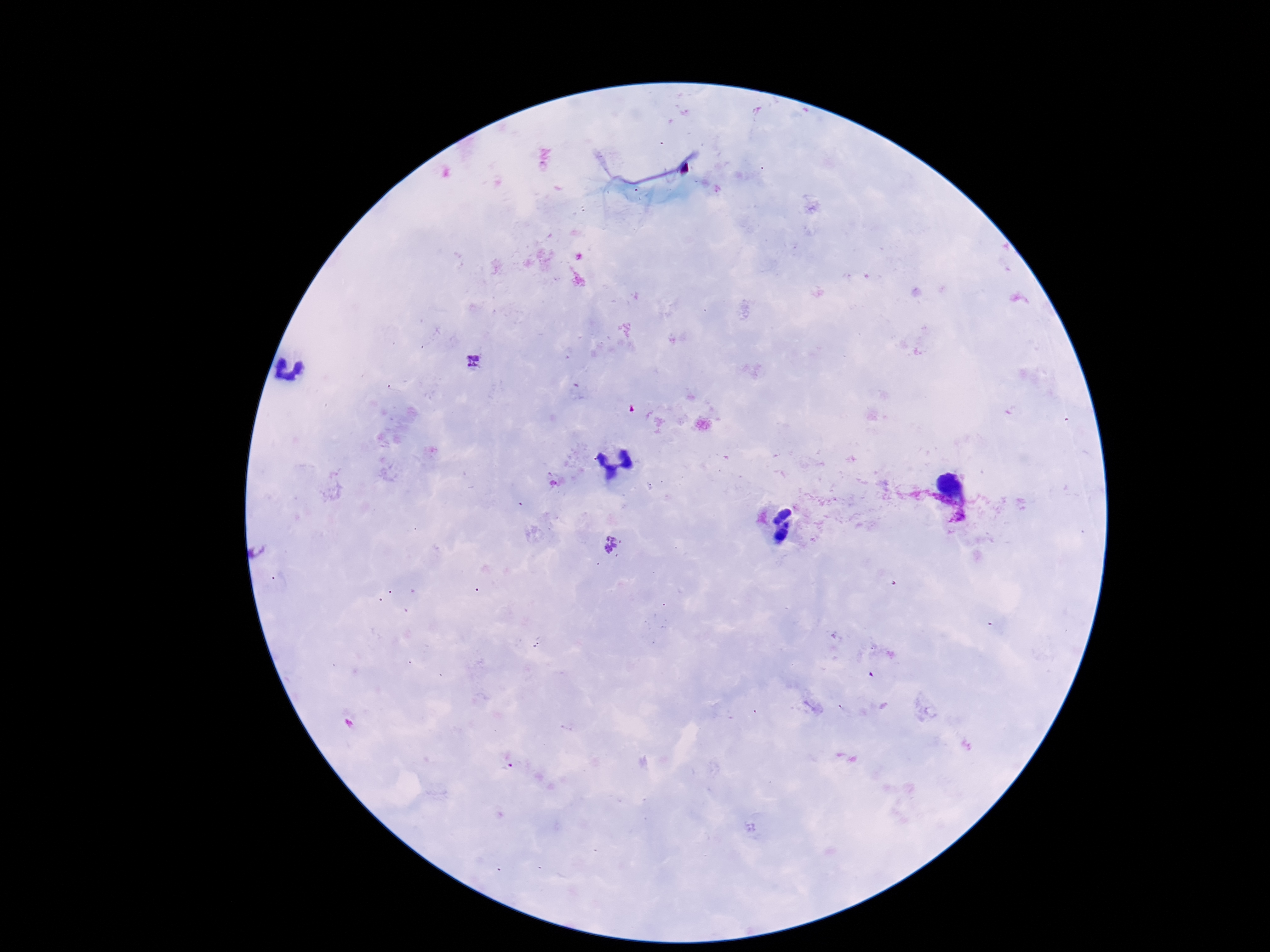

patient malaria status = positive
Plasmodium parasite locations = approximate centers as {x, y} in pixels: {475, 361}, {612, 547}
capture = smartphone camera through the microscope eyepiece
preparation = thick blood smear
stain = Giemsa
magnification = 100x
image size = 1270×952 pixels
field of view = single